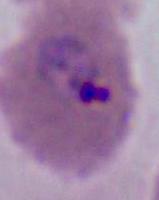

Captured at either 400x or 1000x magnification. Photomicrograph. A Plasmodium parasite is seen.